Name the cell type shown.
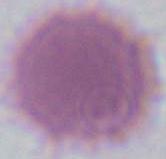
This is an erythrocyte.

Micrograph. Captured at 1000x magnification.